Identify the blood parasite species.
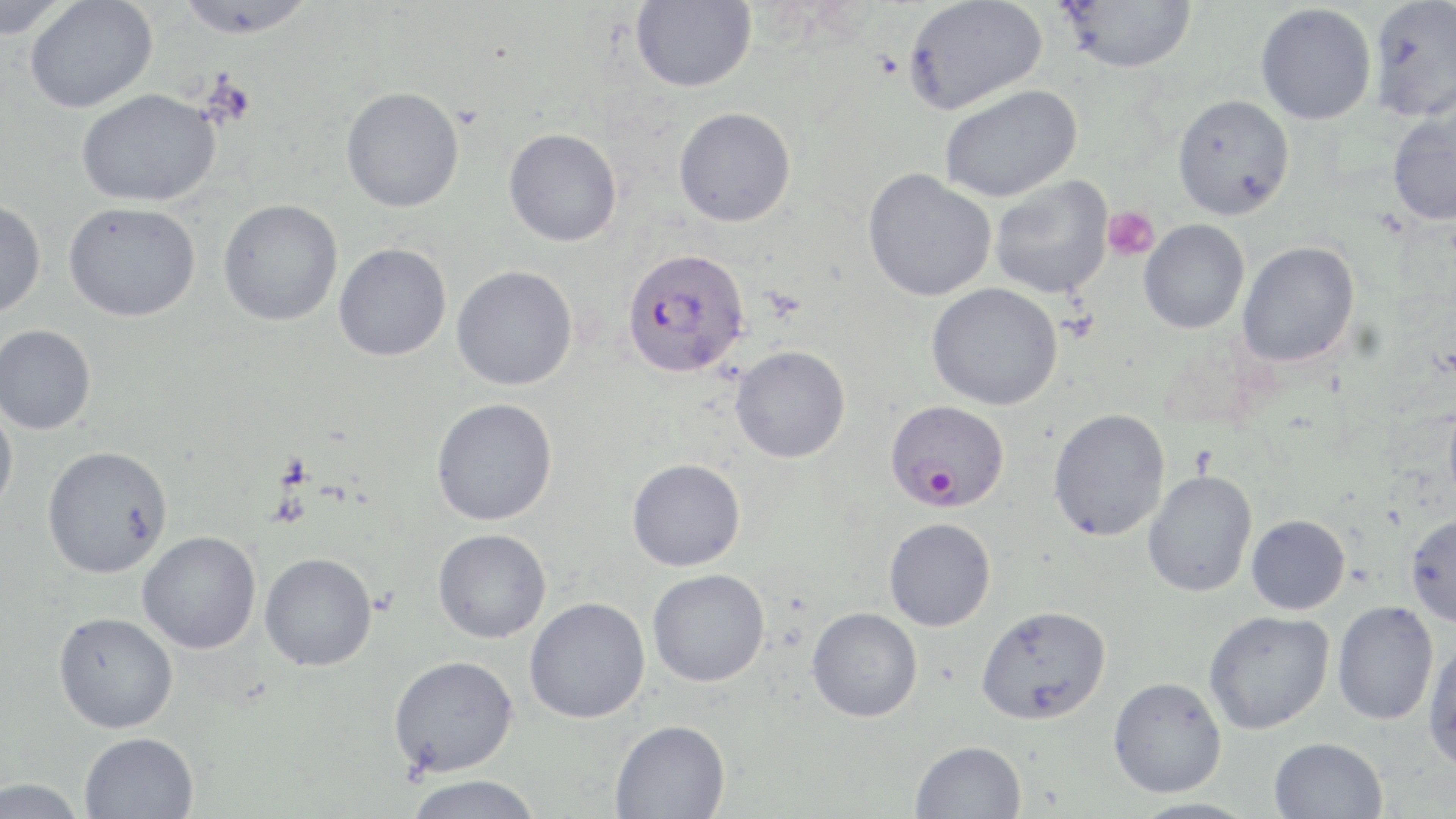

Plasmodium falciparum.

Summary:
  - Coordinate format: approximate bounding boxes as named x1/y1/x2/y2 corners in pixels
  - Platelet locations: (x1=1102, y1=207, x2=1160, y2=261)
  - Plasmodium falciparum-infected red blood cell locations: (x1=621, y1=247, x2=750, y2=378), (x1=888, y1=399, x2=1007, y2=511)
  - Uninfected red blood cell locations: (x1=0, y1=0, x2=72, y2=39), (x1=25, y1=0, x2=157, y2=113), (x1=176, y1=0, x2=318, y2=39), (x1=1059, y1=0, x2=1196, y2=73), (x1=1367, y1=0, x2=1456, y2=122), (x1=630, y1=1, x2=756, y2=92), (x1=903, y1=1, x2=1047, y2=115), (x1=1256, y1=3, x2=1376, y2=125), (x1=939, y1=84, x2=1082, y2=202), (x1=341, y1=86, x2=464, y2=212), (x1=76, y1=88, x2=220, y2=207), (x1=1172, y1=94, x2=1295, y2=220), (x1=673, y1=107, x2=796, y2=227), (x1=1387, y1=108, x2=1456, y2=226), (x1=504, y1=128, x2=622, y2=246), (x1=862, y1=169, x2=996, y2=301), (x1=990, y1=176, x2=1113, y2=298), (x1=0, y1=199, x2=46, y2=317), (x1=218, y1=200, x2=343, y2=326), (x1=63, y1=201, x2=201, y2=321), (x1=1139, y1=219, x2=1249, y2=334), (x1=1237, y1=241, x2=1360, y2=367), (x1=333, y1=242, x2=451, y2=361), (x1=452, y1=265, x2=578, y2=390), (x1=926, y1=282, x2=1063, y2=410), (x1=0, y1=324, x2=96, y2=434), (x1=730, y1=345, x2=850, y2=463), (x1=431, y1=398, x2=558, y2=525), (x1=1444, y1=400, x2=1456, y2=511), (x1=0, y1=404, x2=18, y2=514), (x1=1048, y1=408, x2=1169, y2=541), (x1=42, y1=445, x2=173, y2=578), (x1=627, y1=458, x2=745, y2=571), (x1=1143, y1=470, x2=1257, y2=597), (x1=1405, y1=514, x2=1456, y2=626), (x1=1246, y1=515, x2=1350, y2=615), (x1=884, y1=518, x2=996, y2=631), (x1=433, y1=528, x2=551, y2=643), (x1=137, y1=531, x2=261, y2=654), (x1=259, y1=552, x2=377, y2=671), (x1=647, y1=569, x2=770, y2=687), (x1=524, y1=597, x2=650, y2=723), (x1=1332, y1=601, x2=1439, y2=725), (x1=976, y1=604, x2=1111, y2=725), (x1=806, y1=607, x2=923, y2=722), (x1=1203, y1=610, x2=1334, y2=734), (x1=53, y1=611, x2=178, y2=733), (x1=1423, y1=638, x2=1456, y2=775), (x1=388, y1=655, x2=518, y2=777), (x1=1108, y1=677, x2=1227, y2=797), (x1=610, y1=719, x2=730, y2=818), (x1=79, y1=732, x2=200, y2=819), (x1=1269, y1=737, x2=1389, y2=819), (x1=910, y1=740, x2=1027, y2=819), (x1=403, y1=775, x2=544, y2=819), (x1=0, y1=778, x2=87, y2=819), (x1=1126, y1=798, x2=1262, y2=819)
  - Image size: 1456×819 pixels
  - Preparation: thin blood film
  - Magnification: 1000x
  - Field of view: one of a larger specimen
  - Stain: May-Grünwald-Giemsa
  - Modality: light microscopy